Locate every Plasmodium parasite.
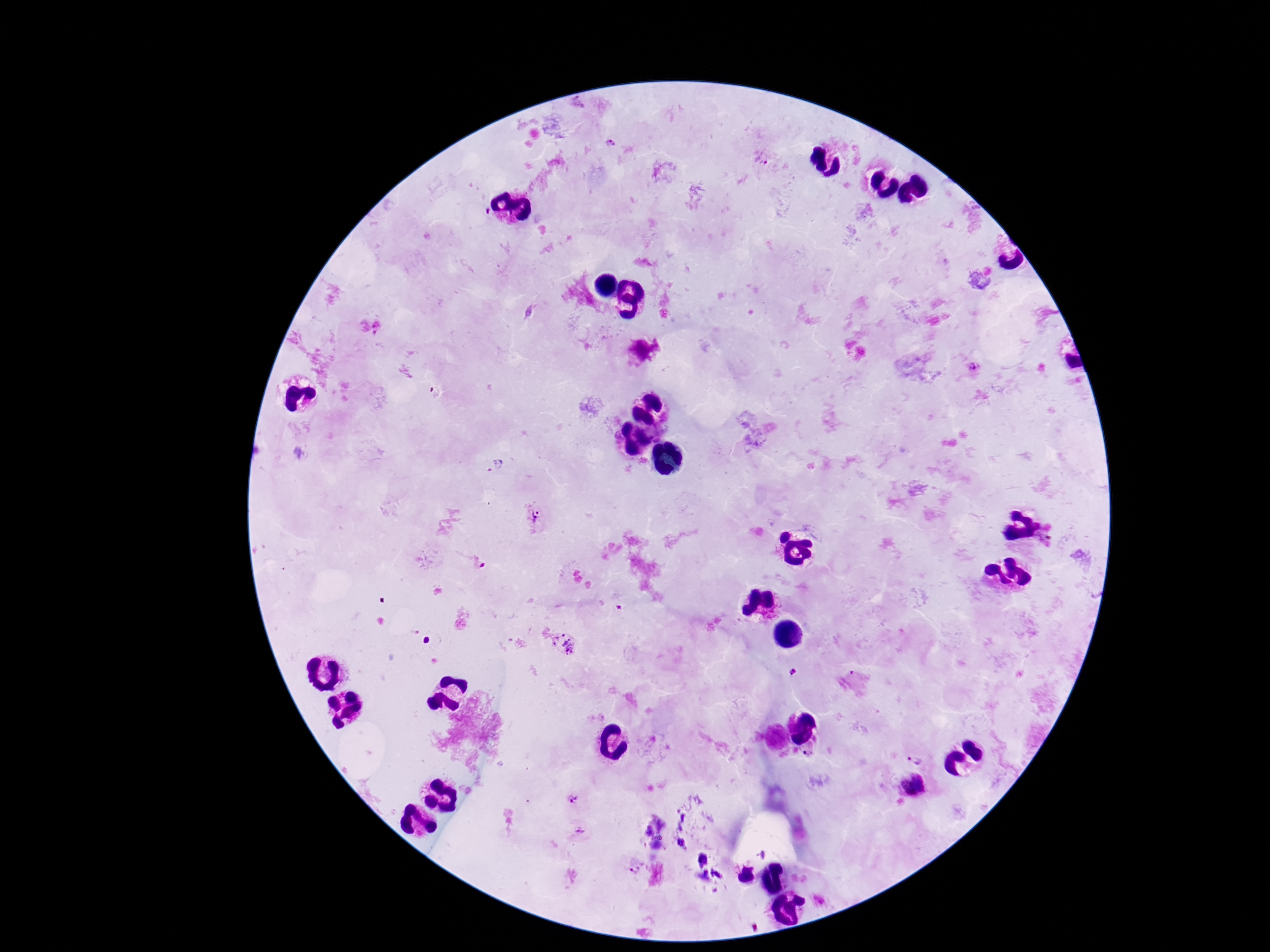

Approximate centers as [x, y] in pixels.
Plasmodium parasites: [610, 144], [763, 159], [972, 367], [532, 517], [472, 562], [563, 643], [793, 672], [916, 758], [574, 799], [637, 866].

Summary:
  - Preparation: thick peripheral-blood smear
  - Stain: Giemsa
  - Patient malaria status: positive
  - Capture: smartphone camera through the microscope eyepiece
  - Image size: 1270×952 pixels
  - Field of view: one from this slide
  - Magnification: 100x